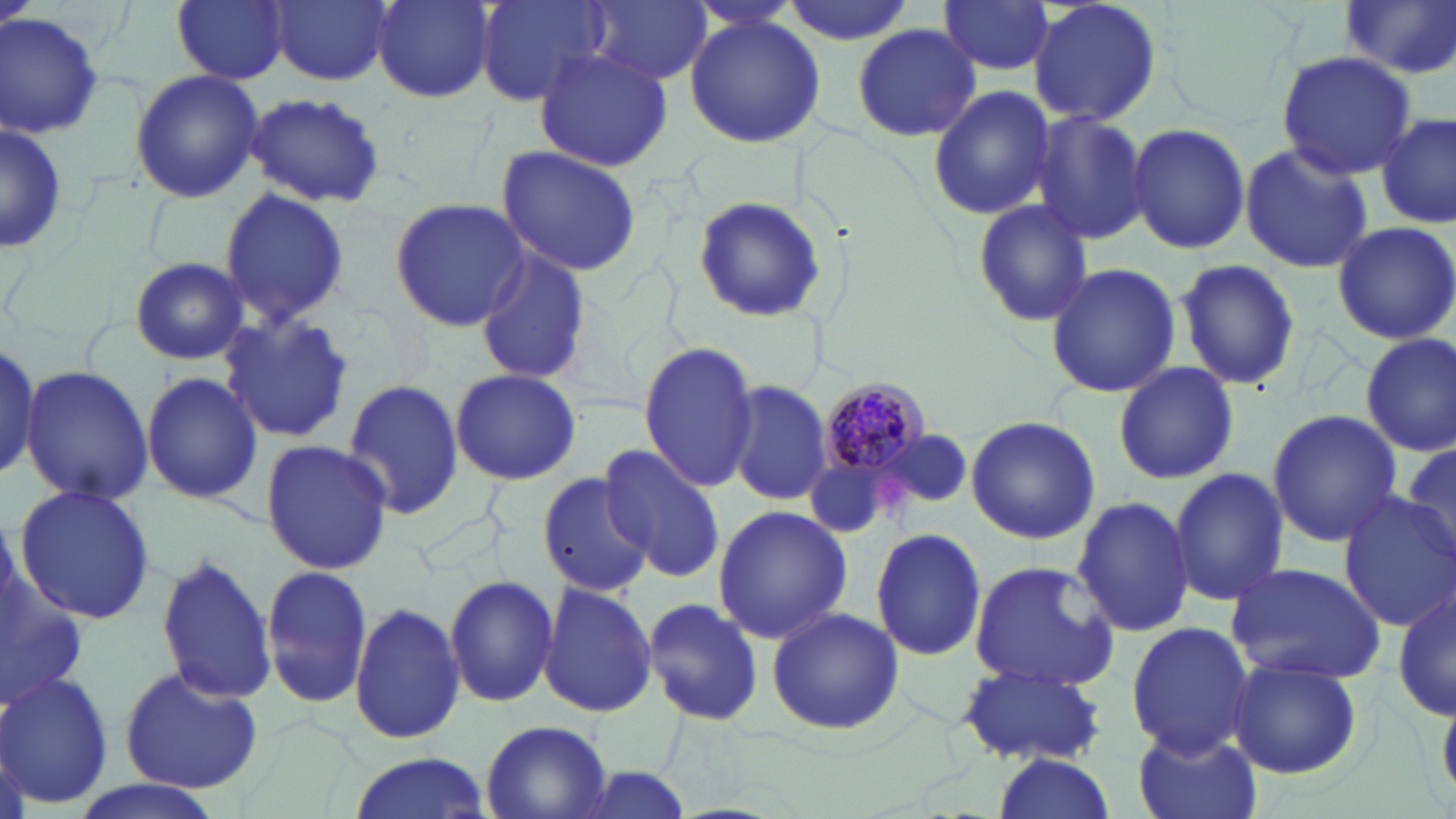

Approximate bounding boxes as named x1/y1/x2/y2 corners in pixels. Uninfected red blood cell locations: (x1=170, y1=0, x2=289, y2=84), (x1=270, y1=0, x2=392, y2=87), (x1=371, y1=0, x2=496, y2=103), (x1=476, y1=0, x2=611, y2=106), (x1=584, y1=0, x2=713, y2=87), (x1=774, y1=0, x2=919, y2=45), (x1=938, y1=0, x2=1059, y2=78), (x1=1026, y1=0, x2=1163, y2=127), (x1=1342, y1=2, x2=1456, y2=79), (x1=0, y1=10, x2=105, y2=139), (x1=685, y1=13, x2=826, y2=149), (x1=848, y1=23, x2=982, y2=142), (x1=534, y1=46, x2=672, y2=174), (x1=1274, y1=51, x2=1418, y2=178), (x1=131, y1=70, x2=264, y2=203), (x1=927, y1=86, x2=1058, y2=220), (x1=242, y1=94, x2=387, y2=208), (x1=1028, y1=110, x2=1150, y2=246), (x1=1377, y1=111, x2=1453, y2=231), (x1=1129, y1=122, x2=1249, y2=254), (x1=0, y1=125, x2=67, y2=252), (x1=1240, y1=142, x2=1374, y2=274), (x1=495, y1=144, x2=644, y2=277), (x1=218, y1=188, x2=351, y2=326), (x1=390, y1=196, x2=527, y2=330), (x1=690, y1=196, x2=828, y2=325), (x1=971, y1=199, x2=1094, y2=326), (x1=1329, y1=221, x2=1456, y2=346), (x1=475, y1=248, x2=591, y2=387), (x1=130, y1=257, x2=250, y2=365), (x1=1175, y1=258, x2=1302, y2=392), (x1=1045, y1=262, x2=1180, y2=397), (x1=218, y1=313, x2=355, y2=444), (x1=1359, y1=333, x2=1456, y2=457), (x1=637, y1=339, x2=759, y2=493), (x1=0, y1=343, x2=44, y2=481), (x1=1112, y1=361, x2=1239, y2=486), (x1=22, y1=366, x2=154, y2=506), (x1=449, y1=369, x2=582, y2=486), (x1=141, y1=371, x2=263, y2=505), (x1=343, y1=379, x2=465, y2=519), (x1=727, y1=380, x2=834, y2=505), (x1=1266, y1=410, x2=1402, y2=544), (x1=965, y1=416, x2=1101, y2=543), (x1=880, y1=430, x2=974, y2=506), (x1=1398, y1=437, x2=1456, y2=564), (x1=260, y1=440, x2=394, y2=575), (x1=599, y1=444, x2=726, y2=583), (x1=1167, y1=466, x2=1288, y2=608), (x1=538, y1=469, x2=656, y2=598), (x1=12, y1=484, x2=156, y2=625), (x1=1334, y1=491, x2=1456, y2=631), (x1=1072, y1=495, x2=1196, y2=638), (x1=714, y1=504, x2=850, y2=644), (x1=871, y1=527, x2=986, y2=662), (x1=153, y1=549, x2=279, y2=706), (x1=967, y1=561, x2=1122, y2=689), (x1=1225, y1=561, x2=1389, y2=685), (x1=260, y1=563, x2=375, y2=711), (x1=0, y1=568, x2=87, y2=720), (x1=443, y1=573, x2=558, y2=709), (x1=538, y1=582, x2=659, y2=720), (x1=1392, y1=584, x2=1455, y2=723), (x1=640, y1=598, x2=765, y2=725), (x1=350, y1=601, x2=466, y2=743), (x1=767, y1=607, x2=903, y2=734), (x1=1124, y1=621, x2=1253, y2=759), (x1=1229, y1=656, x2=1362, y2=781), (x1=955, y1=663, x2=1109, y2=768), (x1=117, y1=665, x2=265, y2=793), (x1=0, y1=673, x2=114, y2=807), (x1=480, y1=721, x2=613, y2=818), (x1=1131, y1=726, x2=1262, y2=819), (x1=345, y1=753, x2=492, y2=818), (x1=987, y1=753, x2=1117, y2=819), (x1=563, y1=767, x2=699, y2=818), (x1=71, y1=779, x2=225, y2=819). Plasmodium malariae-infected red blood cell locations: (x1=817, y1=378, x2=933, y2=481). Slide-level diagnosis: Plasmodium malariae. Optical microscopy. One field of a larger specimen. Image is 1456×819 pixels. May-Grünwald-Giemsa stain. Captured at 1000x magnification. Thin blood smear.